Comment on the morphology of the red blood cells.
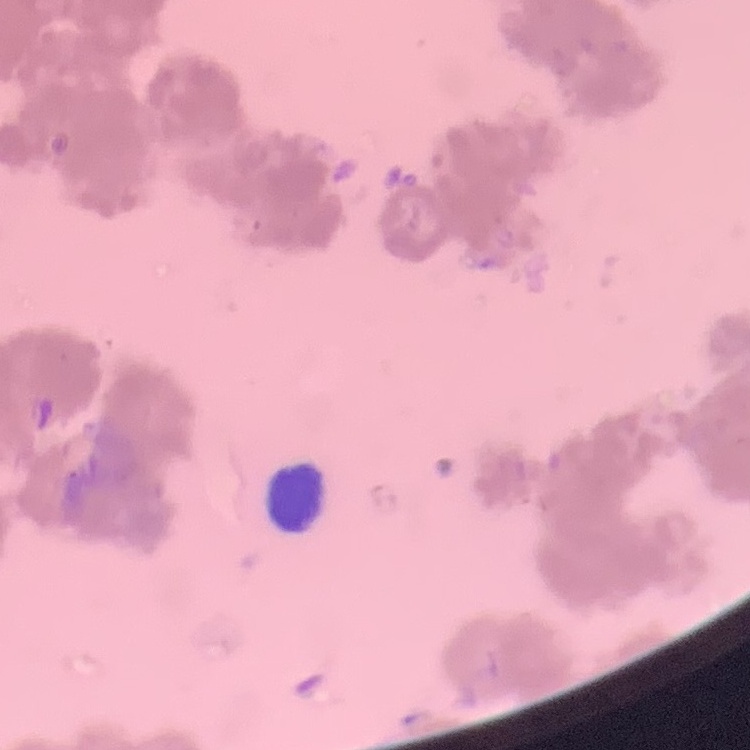

Rouleaux formation.

Summary:
  - Stain: Field's or Giemsa
  - Image type: square crop of a larger photomicrograph
  - Preparation: thin peripheral smear